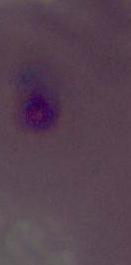
modality = micrograph
magnification = 400x or 1000x
identification = Plasmodium